Identify the parasite.
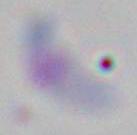
This is Toxoplasma gondii.

Summary:
  - Magnification: 1000x
  - Modality: micrograph